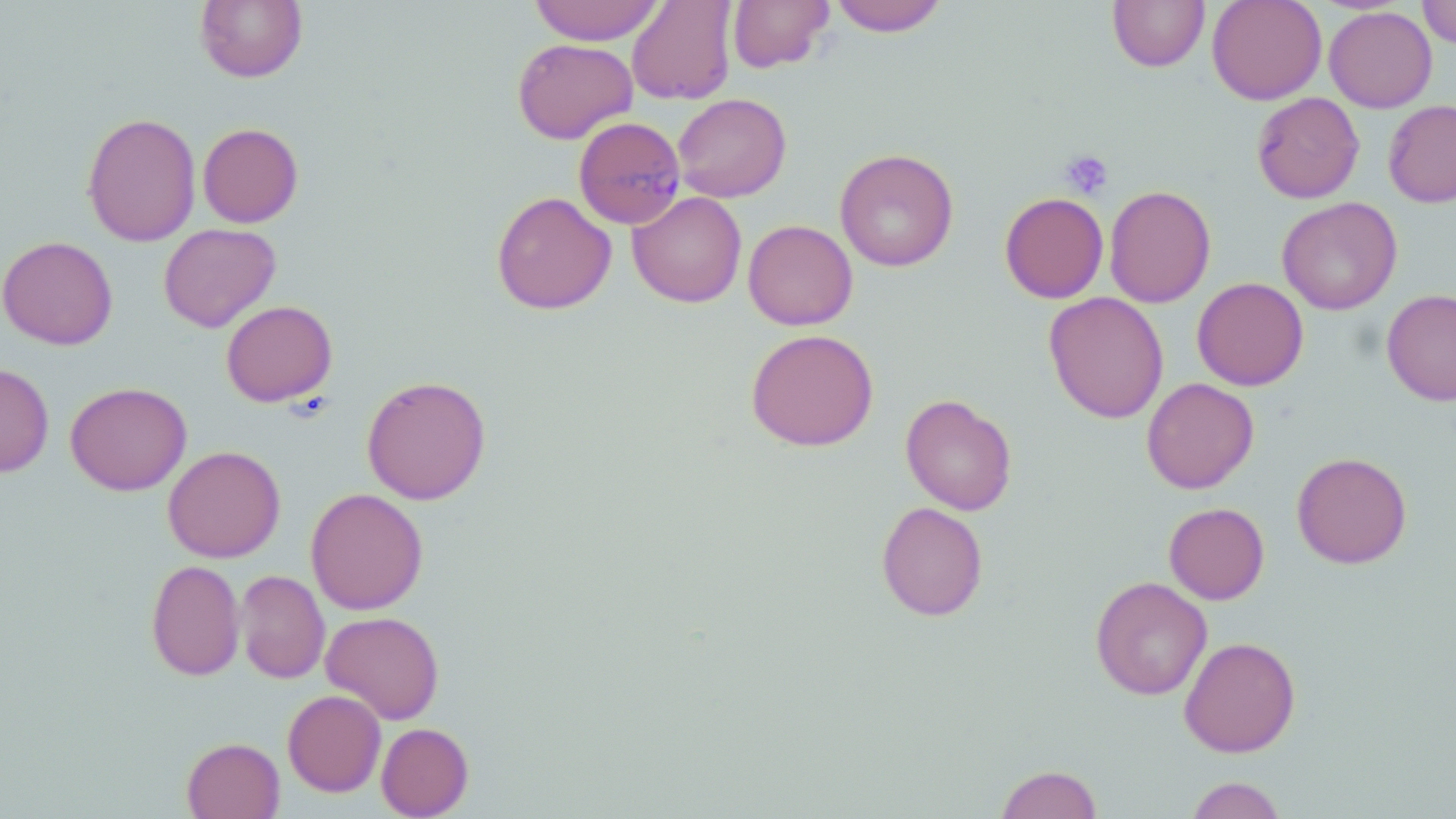
Approximate bounding boxes as named x1/y1/x2/y2 corners in pixels. Platelet locations: (x1=1060, y1=149, x2=1114, y2=200). Plasmodium malariae-infected red blood cell locations: (x1=573, y1=116, x2=686, y2=230). Uninfected red blood cell locations: (x1=194, y1=0, x2=308, y2=83), (x1=529, y1=0, x2=666, y2=45), (x1=626, y1=0, x2=739, y2=105), (x1=727, y1=0, x2=834, y2=73), (x1=828, y1=0, x2=949, y2=36), (x1=1107, y1=0, x2=1209, y2=72), (x1=1207, y1=0, x2=1327, y2=104), (x1=1417, y1=0, x2=1456, y2=48), (x1=1324, y1=6, x2=1437, y2=113), (x1=512, y1=38, x2=638, y2=144), (x1=1252, y1=92, x2=1364, y2=203), (x1=673, y1=93, x2=792, y2=202), (x1=1383, y1=99, x2=1456, y2=207), (x1=81, y1=112, x2=201, y2=246), (x1=198, y1=122, x2=303, y2=228), (x1=834, y1=148, x2=959, y2=272), (x1=1104, y1=185, x2=1216, y2=308), (x1=491, y1=190, x2=616, y2=315), (x1=627, y1=191, x2=747, y2=307), (x1=999, y1=192, x2=1109, y2=303), (x1=1277, y1=197, x2=1402, y2=315), (x1=742, y1=219, x2=858, y2=330), (x1=158, y1=223, x2=281, y2=332), (x1=0, y1=235, x2=118, y2=350), (x1=1193, y1=277, x2=1309, y2=390), (x1=1381, y1=288, x2=1456, y2=406), (x1=1043, y1=291, x2=1169, y2=424), (x1=221, y1=300, x2=337, y2=406), (x1=745, y1=329, x2=878, y2=451), (x1=0, y1=363, x2=54, y2=477), (x1=361, y1=374, x2=491, y2=505), (x1=1141, y1=377, x2=1259, y2=494), (x1=65, y1=382, x2=191, y2=496), (x1=900, y1=393, x2=1018, y2=515), (x1=162, y1=445, x2=285, y2=563), (x1=1291, y1=451, x2=1412, y2=569), (x1=305, y1=488, x2=429, y2=615), (x1=876, y1=501, x2=988, y2=621), (x1=1164, y1=502, x2=1269, y2=604), (x1=146, y1=559, x2=245, y2=681), (x1=236, y1=570, x2=330, y2=684), (x1=1090, y1=576, x2=1213, y2=700), (x1=321, y1=610, x2=444, y2=724), (x1=1178, y1=636, x2=1301, y2=758), (x1=283, y1=689, x2=386, y2=796), (x1=376, y1=722, x2=473, y2=818), (x1=181, y1=737, x2=285, y2=819), (x1=995, y1=764, x2=1103, y2=819), (x1=1185, y1=776, x2=1288, y2=819). Slide-level diagnosis: Plasmodium malariae. May-Grünwald-Giemsa stain. 1000x magnification. Image is 1456×819 pixels. Thin blood smear. Single field of view. Light microscopy.